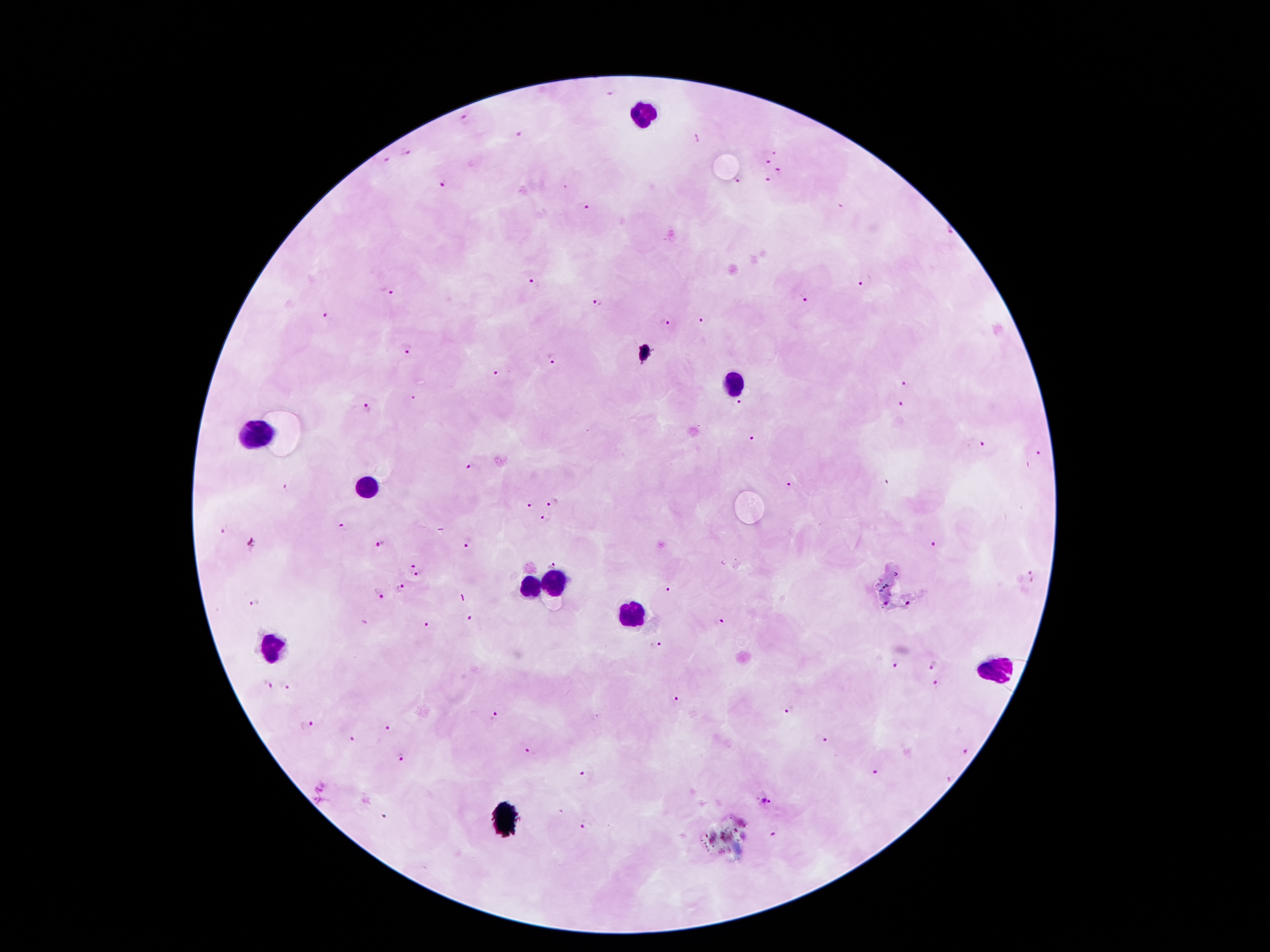

Approximate centers as [x, y] in pixels.
Summary:
  - Leukocyte locations: [647, 113], [735, 385], [258, 431], [368, 484], [551, 582], [530, 589], [631, 610], [272, 649], [997, 669]
  - Malaria parasite locations: [611, 95], [464, 119], [518, 136], [406, 151], [774, 154], [386, 161], [767, 161], [777, 171], [766, 179], [736, 181], [441, 183], [587, 208], [949, 232], [535, 282], [861, 285], [386, 293], [805, 299], [596, 303], [325, 315], [700, 321], [666, 323], [408, 349], [553, 359], [497, 373], [904, 382], [413, 398], [739, 404], [366, 406], [902, 406], [753, 439], [981, 444], [1038, 455], [471, 467], [887, 483], [789, 485], [284, 487], [552, 500], [531, 504], [547, 519], [343, 526], [224, 529], [935, 543], [468, 545], [252, 546], [381, 546], [413, 562], [552, 562], [1030, 572], [417, 574], [400, 589], [670, 590], [379, 594], [255, 603], [471, 619], [720, 622], [427, 625], [656, 647], [935, 665], [896, 666], [269, 685], [935, 685], [286, 687], [677, 700], [790, 710], [495, 716], [308, 726], [388, 728], [824, 739], [352, 740], [530, 751], [967, 751], [401, 758], [875, 772], [584, 773], [948, 779], [764, 803], [384, 816], [585, 824], [773, 834]
  - Capture: smartphone camera through the microscope eyepiece
  - Preparation: thick peripheral-blood smear
  - Stain: Giemsa
  - Patient malaria status: positive for Plasmodium falciparum
  - Field of view: one from this slide
  - Magnification: 100x
  - Image size: 1270×952 pixels